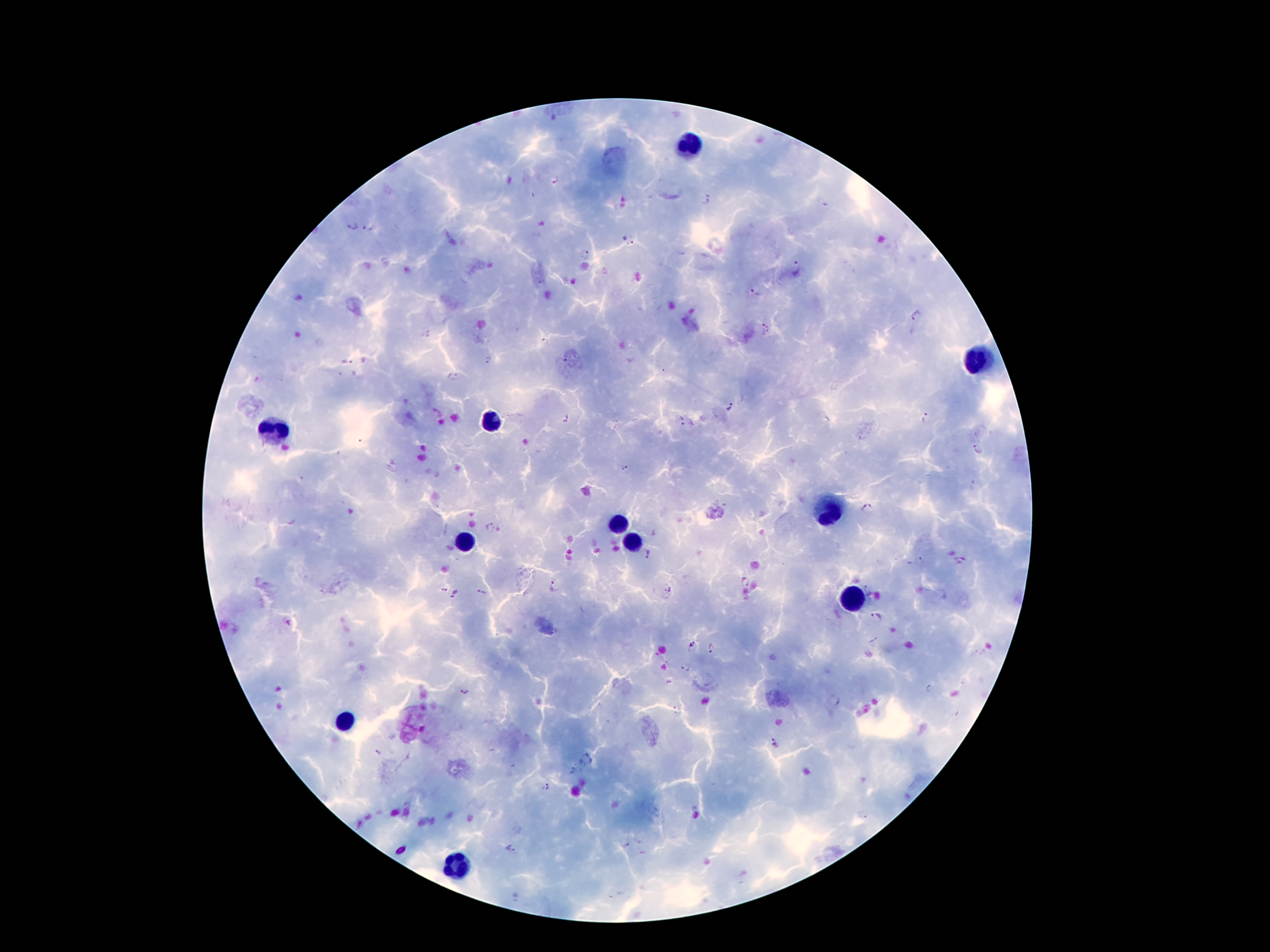
Approximate centers as {x, y} in pixels.
Summary:
  - Leukocyte locations: {693, 149}, {974, 362}, {486, 421}, {273, 431}, {829, 512}, {618, 526}, {461, 544}, {631, 544}, {852, 598}, {343, 723}, {459, 867}
  - Plasmodium parasite locations: {557, 180}, {707, 200}, {820, 204}, {352, 226}, {369, 228}, {632, 241}, {585, 256}, {796, 268}, {755, 291}, {915, 316}, {544, 343}, {490, 361}, {345, 362}, {453, 377}, {729, 409}, {566, 416}, {926, 416}, {681, 421}, {978, 450}, {624, 466}, {866, 507}, {491, 527}, {650, 554}, {919, 560}, {745, 582}, {554, 585}, {445, 590}, {670, 590}, {482, 592}, {456, 594}, {876, 616}, {693, 646}, {712, 647}, {685, 668}, {931, 689}, {465, 691}, {676, 709}, {774, 743}, {378, 752}, {589, 759}, {546, 787}, {861, 812}, {511, 849}
  - Preparation: thick blood smear
  - Stain: Giemsa
  - Capture: smartphone through the microscope eyepiece
  - Image size: 1270×952 pixels
  - Magnification: 100x
  - Patient malaria status: positive for Plasmodium falciparum
  - Field of view: single